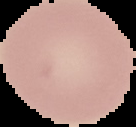

From a thin blood smear. Result: negative for malaria parasites. Image is 136×127 pixels. Segmented cell region on a black background.